Give the position of every leukocyte visible.
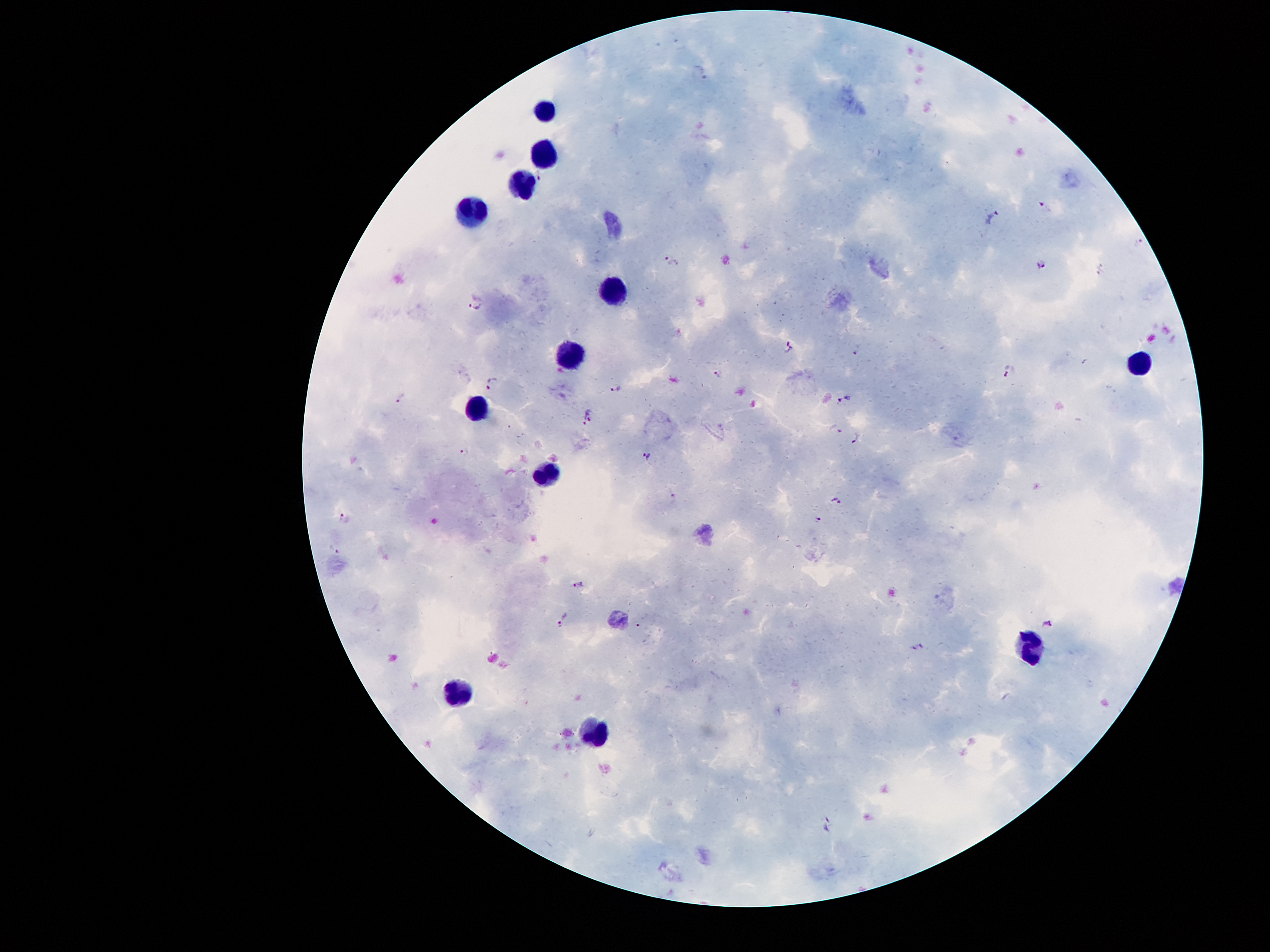
Approximate centers as {x, y} in pixels.
Leukocytes: {547, 109}, {545, 153}, {522, 182}, {475, 210}, {616, 288}, {569, 356}, {1139, 364}, {479, 408}, {548, 474}, {1032, 647}, {459, 698}, {598, 731}.

Malaria parasite locations: {703, 71}, {541, 176}, {1044, 205}, {993, 217}, {1138, 242}, {672, 261}, {1043, 264}, {478, 305}, {788, 344}, {857, 349}, {1009, 371}, {719, 373}, {493, 382}, {616, 389}, {401, 398}, {846, 401}, {591, 411}, {585, 423}, {834, 428}, {856, 439}, {464, 450}, {647, 457}, {672, 494}, {836, 501}, {344, 517}, {817, 520}, {334, 549}, {578, 584}, {563, 617}, {1048, 624}, {918, 647}. Image is 1270×952 pixels. 100x magnification. One field from this slide. Thick blood smear. Giemsa stain. Patient malaria status: infected with Plasmodium falciparum. Photographed through the microscope eyepiece with a smartphone camera.